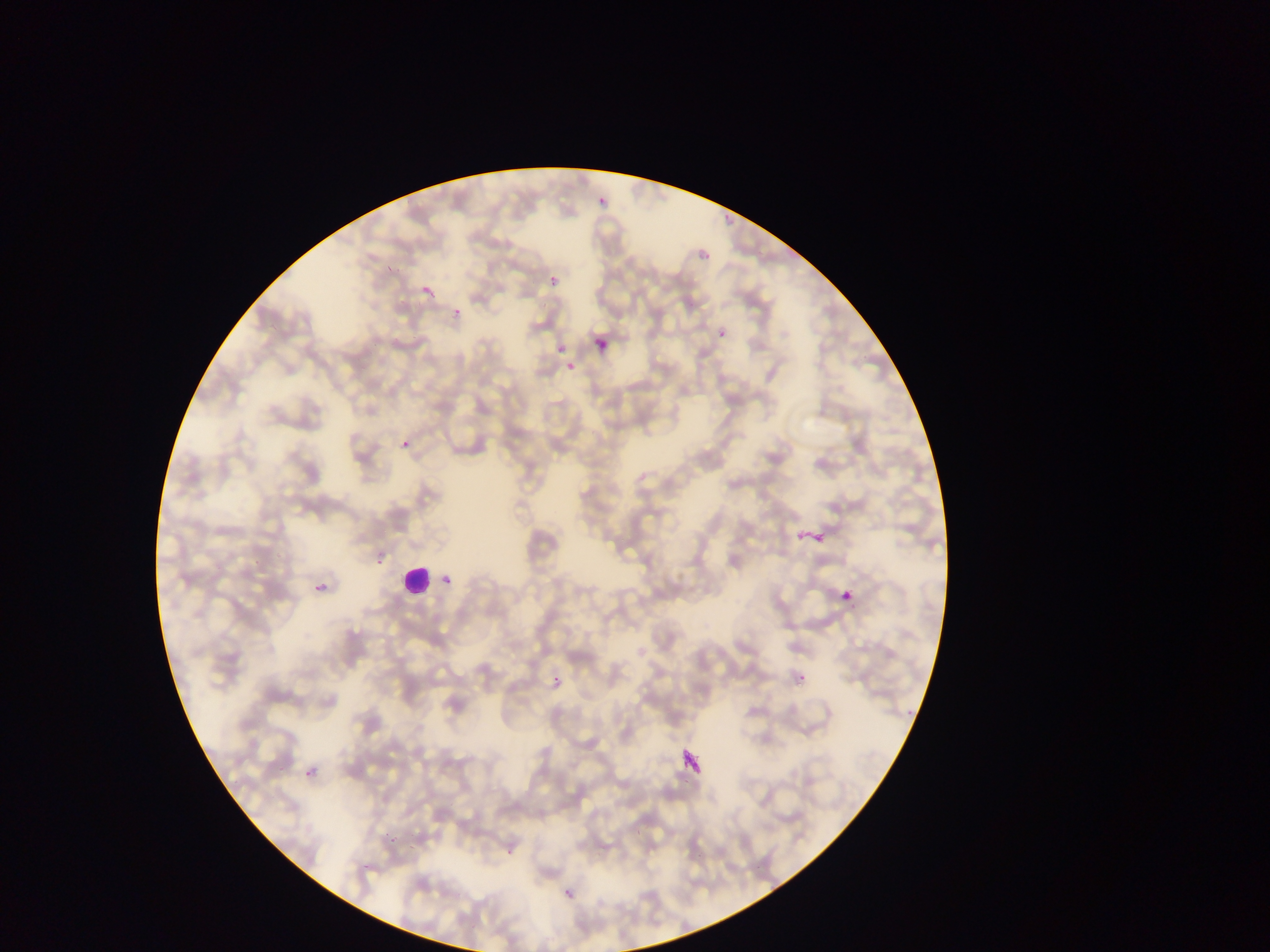

Approximate bounding boxes as (left, top, right, bottom) in pixels.
Summary:
  - Malaria parasite locations: (595, 194, 609, 210), (721, 209, 735, 223), (696, 249, 709, 261), (381, 258, 399, 272), (547, 274, 561, 289), (419, 284, 435, 300), (453, 306, 463, 318), (715, 327, 730, 344), (593, 336, 610, 353), (554, 343, 565, 353), (562, 361, 577, 378), (566, 362, 576, 373), (401, 440, 410, 449), (800, 522, 836, 556), (308, 557, 341, 597), (375, 557, 387, 566), (440, 572, 457, 591), (836, 584, 860, 610), (799, 670, 808, 683), (548, 672, 567, 694), (905, 709, 912, 719), (676, 746, 712, 784), (301, 764, 320, 785), (385, 832, 397, 845), (408, 846, 414, 856), (503, 850, 514, 858), (360, 863, 367, 872), (559, 885, 580, 908)
  - Leukocyte locations: (399, 563, 434, 599)
  - Image size: 1270×952 pixels
  - Country: Ghana
  - Capture: mobile-phone photograph through a microscope
  - Field of view: single
  - Preparation: thin blood smear